Report the malaria status of this cell.
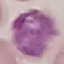

It is parasitized.

Summary:
  - Image type: automatically extracted cell patch, resized to 64 × 64 pixels
  - Preparation: thin smear
  - Capture: smartphone camera at the microscope eyepiece
  - Stain: Giemsa